Name the blood parasite species.
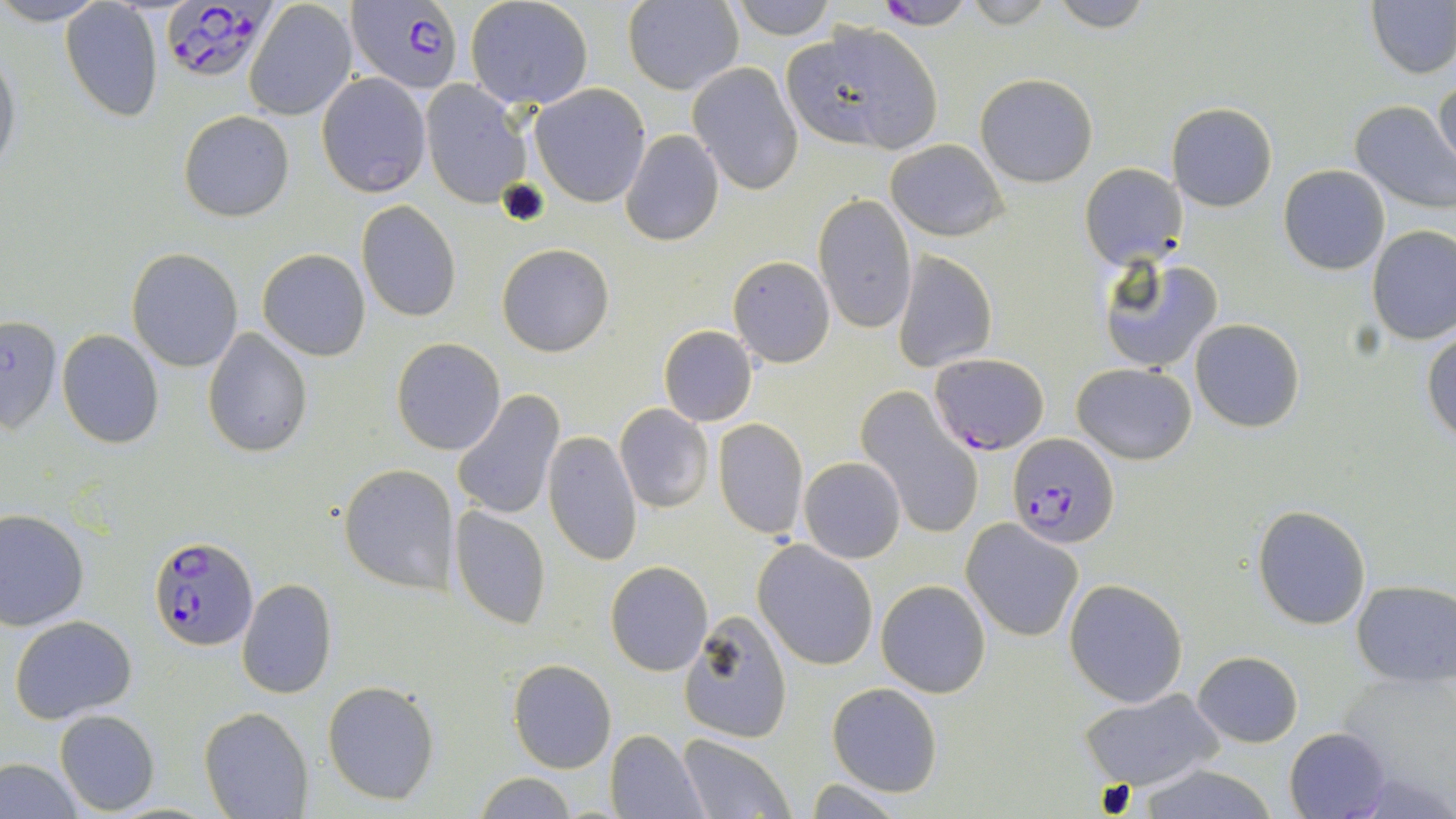

Plasmodium falciparum.

Approximate bounding boxes as [x1, y1, x2, y2] in pixels. Uninfected red blood cell locations: [0, 0, 109, 26], [465, 0, 594, 111], [622, 0, 744, 94], [727, 0, 837, 40], [960, 0, 1060, 29], [1044, 0, 1156, 32], [1368, 0, 1456, 78], [243, 1, 357, 120], [60, 2, 166, 124], [780, 21, 943, 155], [0, 37, 22, 187], [687, 63, 803, 195], [976, 72, 1097, 187], [316, 73, 432, 196], [1434, 77, 1456, 178], [422, 78, 533, 211], [1405, 82, 1454, 190], [530, 83, 651, 207], [1350, 101, 1456, 211], [1166, 102, 1277, 211], [178, 110, 295, 223], [621, 130, 724, 246], [887, 139, 1007, 240], [1080, 163, 1186, 269], [1279, 165, 1390, 275], [814, 194, 917, 333], [356, 201, 461, 321], [1366, 227, 1456, 344], [497, 243, 614, 356], [127, 246, 242, 370], [258, 248, 371, 360], [892, 250, 997, 373], [729, 255, 835, 367], [1097, 255, 1223, 373], [0, 315, 63, 435], [1190, 319, 1306, 433], [659, 325, 758, 426], [202, 328, 313, 457], [56, 329, 165, 449], [1423, 330, 1456, 443], [391, 338, 506, 455], [1072, 362, 1197, 464], [858, 389, 982, 535], [450, 390, 564, 521], [615, 404, 714, 514], [712, 417, 809, 540], [543, 431, 642, 565], [799, 456, 906, 563], [338, 462, 458, 594], [447, 503, 551, 632], [1253, 505, 1371, 629], [0, 508, 89, 630], [962, 519, 1083, 642], [754, 541, 878, 670], [605, 560, 713, 676], [236, 578, 337, 699], [877, 579, 989, 698], [1064, 579, 1188, 707], [1352, 580, 1456, 686], [677, 613, 794, 741], [10, 615, 137, 725], [1193, 652, 1303, 747], [508, 658, 616, 773], [322, 680, 440, 805], [827, 682, 942, 797], [1081, 688, 1226, 790], [202, 708, 313, 818], [55, 709, 160, 814], [1284, 727, 1391, 818], [606, 729, 709, 818], [675, 734, 795, 818], [0, 757, 83, 818], [1127, 763, 1284, 819], [473, 771, 579, 818], [803, 778, 911, 816]. Plasmodium falciparum-infected red blood cell locations: [869, 0, 981, 30], [161, 1, 273, 83], [346, 1, 464, 96], [931, 353, 1049, 456], [1007, 432, 1119, 550], [148, 535, 258, 650]. 1000x magnification. Optical microscopy. One field of a larger specimen. May-Grünwald-Giemsa stain. Thin blood film. Image is 1456×819 pixels.